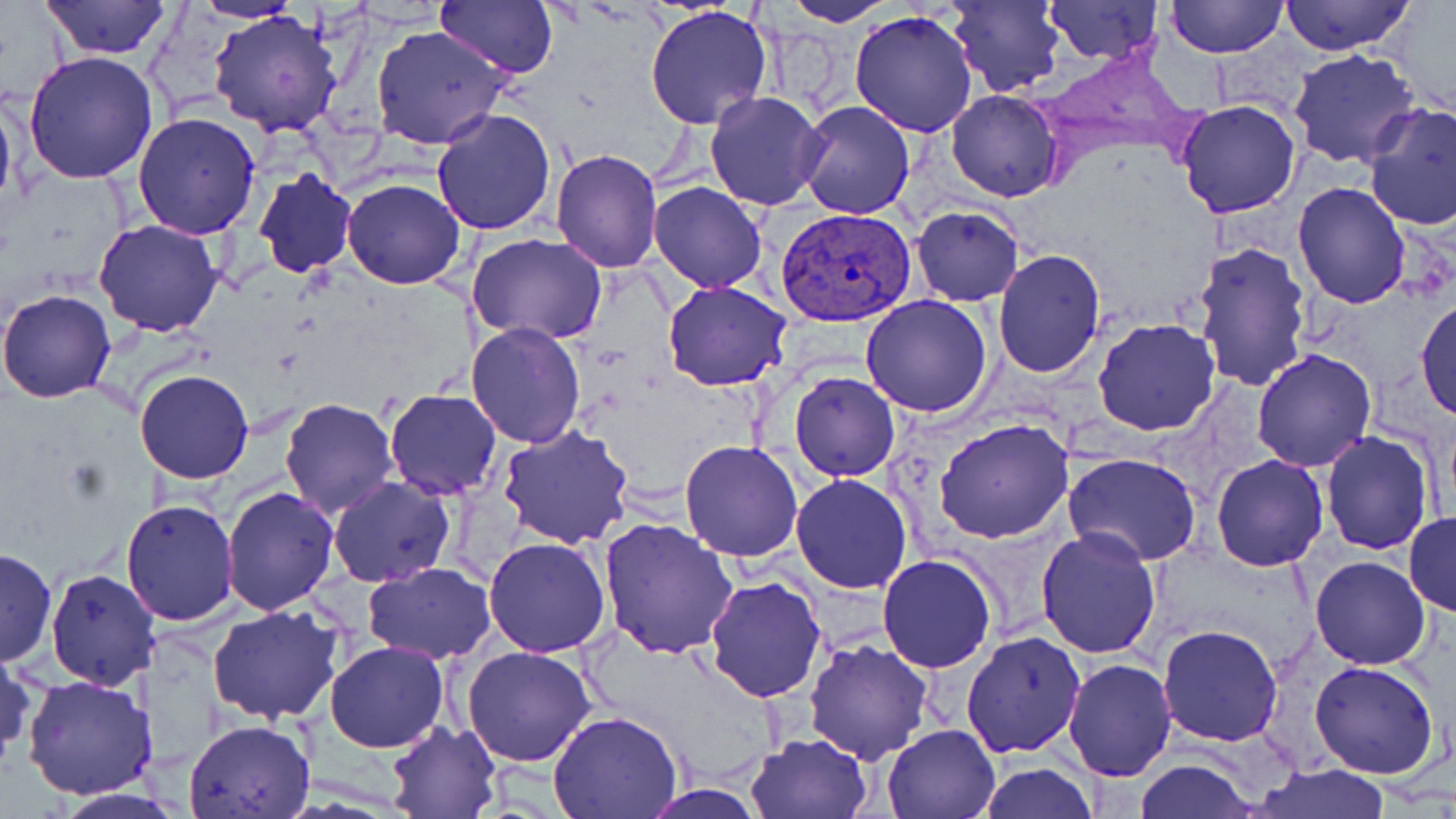
Approximate bounding boxes as (x1,y1)-(x2,y2) corner pairs in pixels. Uninfected red blood cell locations: (434,0)-(560,80), (780,0)-(898,25), (1042,0)-(1165,66), (1167,0)-(1287,59), (1278,0)-(1415,55), (42,1)-(171,60), (188,1)-(309,23), (947,1)-(1064,98), (645,5)-(773,131), (209,9)-(344,137), (849,9)-(980,139), (369,24)-(512,150), (1289,48)-(1419,169), (23,51)-(158,184), (0,89)-(17,220), (703,91)-(828,211), (946,91)-(1064,202), (1176,99)-(1303,219), (795,101)-(917,219), (1363,102)-(1456,232), (433,107)-(557,237), (133,113)-(262,239), (549,149)-(662,273), (252,167)-(359,278), (342,178)-(465,289), (1293,181)-(1410,308), (650,182)-(767,291), (910,207)-(1024,307), (95,218)-(224,337), (467,233)-(609,345), (1192,240)-(1313,392), (993,250)-(1106,376), (663,279)-(792,391), (0,288)-(118,403), (860,294)-(993,418), (1414,294)-(1455,421), (1094,319)-(1220,436), (466,322)-(587,447), (1251,347)-(1377,471), (134,368)-(254,484), (788,371)-(899,482), (384,388)-(503,498), (279,397)-(397,518), (935,419)-(1073,544), (498,426)-(634,548), (1321,430)-(1435,556), (679,440)-(804,561), (1064,453)-(1203,567), (1211,455)-(1327,572), (790,473)-(912,593), (329,476)-(455,586), (221,486)-(338,614), (121,499)-(237,626), (1405,510)-(1455,616), (599,516)-(737,658), (1036,527)-(1162,660), (484,536)-(611,657), (1,547)-(57,666), (878,554)-(998,673), (1310,556)-(1430,670), (362,563)-(496,663), (44,568)-(160,690), (704,573)-(826,702), (208,604)-(346,725), (1158,625)-(1285,747), (960,629)-(1086,757), (803,638)-(932,763), (325,641)-(449,752), (1,642)-(35,765), (463,644)-(597,767), (1062,658)-(1178,781), (1308,660)-(1441,780), (22,674)-(159,800), (548,712)-(681,819), (182,719)-(314,819), (385,720)-(503,818), (882,722)-(1001,817), (745,733)-(874,819), (1133,759)-(1258,818), (978,761)-(1097,818), (1249,764)-(1389,818), (637,786)-(768,818). Plasmodium vivax-infected red blood cell locations: (778,207)-(917,327). Slide-level diagnosis: Plasmodium vivax. Image is 1456×819 pixels. Captured at 1000x magnification. One field of a larger specimen. May-Grünwald-Giemsa-stained preparation. Thin blood smear. Light microscopy.